Name the parasite shown.
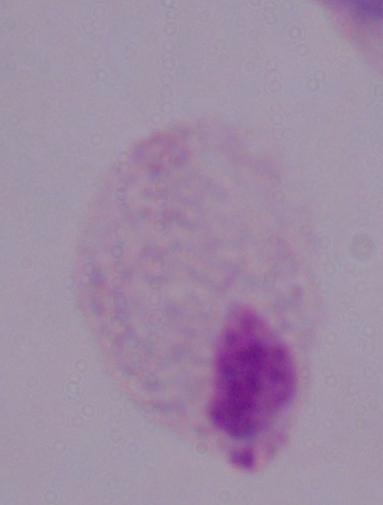

A trichomonad.

{
  "modality": "micrograph",
  "magnification": "1000x"
}